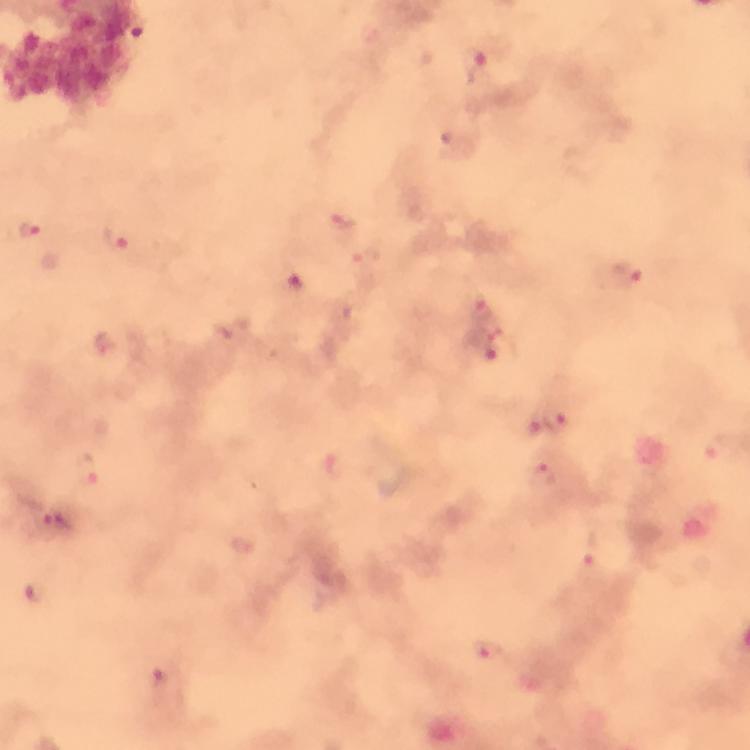

capture = smartphone photograph through a microscope
Plasmodium parasite locations = approximate centers as [x, y] in pixels: [475, 64], [458, 143], [341, 223], [30, 230], [117, 240], [625, 276], [297, 290], [482, 311], [106, 343], [483, 346], [557, 420], [86, 471], [543, 476], [53, 523], [592, 569], [35, 592], [489, 654], [167, 685]
stain = Giemsa
immersion oil = used
context = from a diagnostic examination for malaria
cropped from = one field of view
preparation = thick blood smear
magnification = 100x
image size = 750×750 pixels